Name the parasite shown.
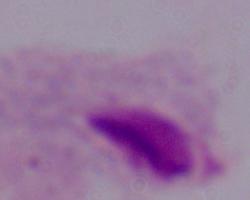
A trichomonad.

Micrograph. Captured at 1000x magnification.